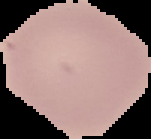

Malaria status: uninfected. Segmented cell region on a black background. From a thin blood film. Image is 151×139 pixels.